Classify this cell by malaria status.
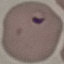

Parasitized.

image type = cell patch, automatically extracted from a larger field of view and resized to 64 × 64 pixels
preparation = thin smear
stain = Giemsa
capture = smartphone through the microscope eyepiece